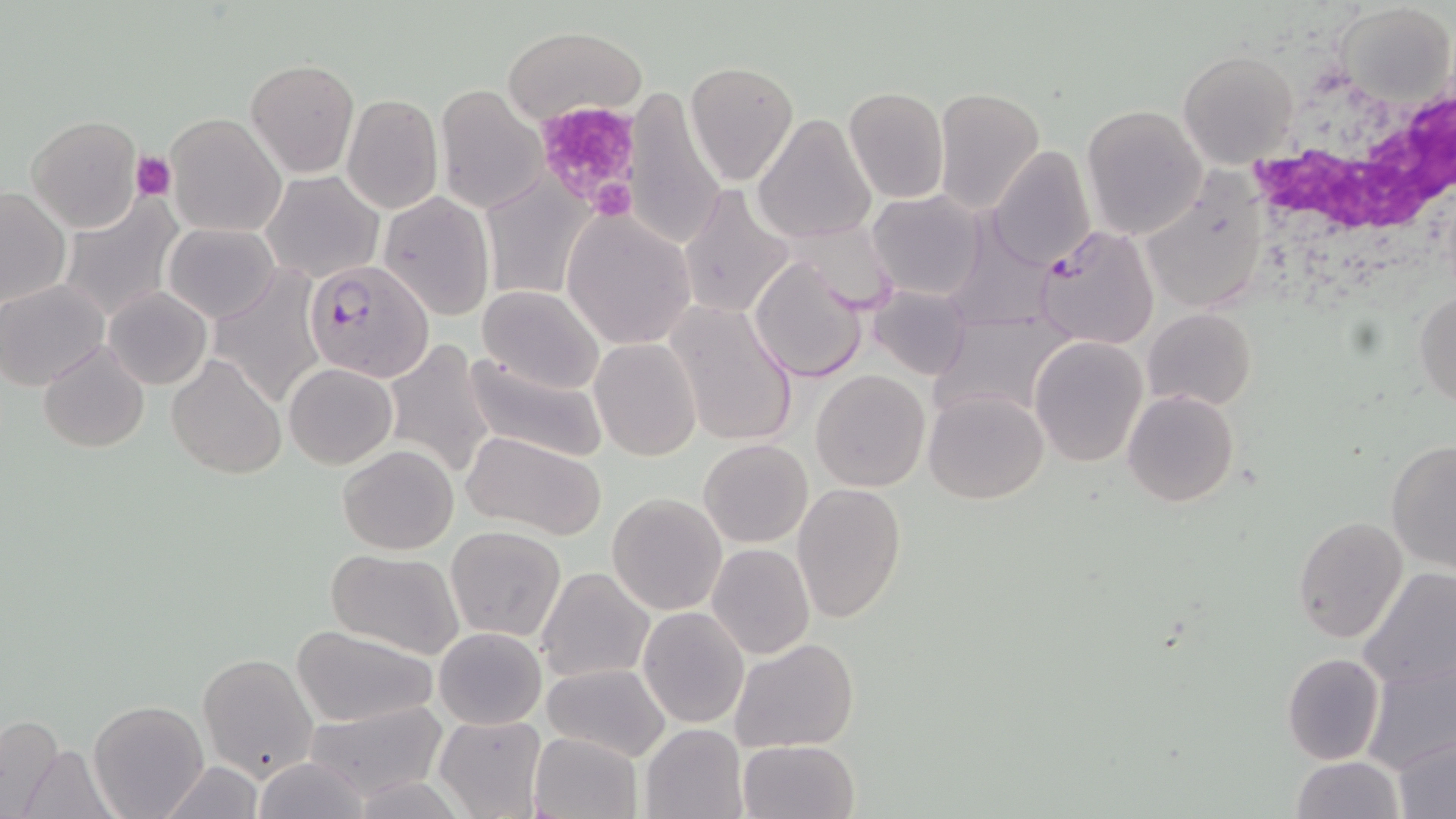

Summary:
  - Coordinate format: approximate bounding boxes as (x1, y1, x2, y2) in pixels
  - White blood cell locations: (1237, 71, 1456, 256)
  - Plasmodium falciparum-infected red blood cell locations: (1034, 224, 1161, 351), (305, 259, 434, 382)
  - Platelet locations: (531, 99, 646, 215), (131, 151, 176, 200)
  - Uninfected red blood cell locations: (1336, 3, 1455, 110), (501, 25, 646, 126), (1178, 50, 1300, 169), (246, 58, 359, 177), (686, 61, 797, 183), (435, 83, 548, 214), (623, 86, 727, 250), (843, 87, 950, 204), (932, 87, 1045, 217), (341, 94, 443, 213), (1081, 105, 1208, 238), (164, 112, 285, 237), (751, 112, 875, 246), (25, 114, 145, 233), (987, 144, 1096, 269), (262, 171, 383, 283), (1141, 174, 1271, 315), (478, 175, 598, 302), (678, 183, 796, 321), (1, 186, 71, 309), (868, 190, 988, 302), (378, 191, 496, 321), (57, 193, 183, 324), (561, 209, 696, 350), (164, 222, 280, 323), (748, 254, 870, 382), (209, 270, 328, 393), (0, 280, 109, 389), (477, 285, 605, 394), (868, 285, 975, 381), (105, 286, 213, 389), (1413, 289, 1456, 407), (663, 300, 800, 448), (927, 307, 1077, 423), (1143, 307, 1256, 412), (1027, 335, 1149, 468), (384, 338, 498, 480), (589, 338, 702, 461), (38, 340, 150, 453), (462, 352, 609, 463), (166, 355, 286, 479), (285, 363, 396, 468), (810, 370, 930, 492), (1122, 389, 1240, 508), (924, 390, 1049, 504), (461, 429, 606, 539), (699, 438, 812, 547), (1385, 438, 1456, 572), (337, 444, 458, 555), (791, 482, 907, 623), (606, 492, 728, 614), (1294, 515, 1408, 643), (443, 524, 567, 643), (706, 543, 814, 659), (323, 548, 466, 659), (535, 567, 655, 684), (1356, 568, 1456, 694), (638, 606, 750, 729), (290, 624, 442, 728), (433, 626, 547, 730), (729, 637, 859, 753), (1281, 652, 1386, 765), (197, 654, 319, 782), (1360, 654, 1455, 777), (541, 664, 671, 763), (88, 698, 209, 819), (305, 699, 449, 803), (434, 713, 547, 819), (0, 715, 66, 819), (640, 722, 749, 819), (1394, 731, 1455, 817), (529, 732, 642, 819), (12, 738, 120, 818), (737, 739, 860, 819), (252, 756, 373, 818), (1289, 756, 1404, 819), (157, 761, 268, 816)
  - Slide-level diagnosis: Plasmodium falciparum
  - Modality: optical microscopy
  - Magnification: 1000x
  - Image size: 1456×819 pixels
  - Stain: May-Grünwald-Giemsa
  - Preparation: thin blood smear
  - Field of view: one of a larger specimen